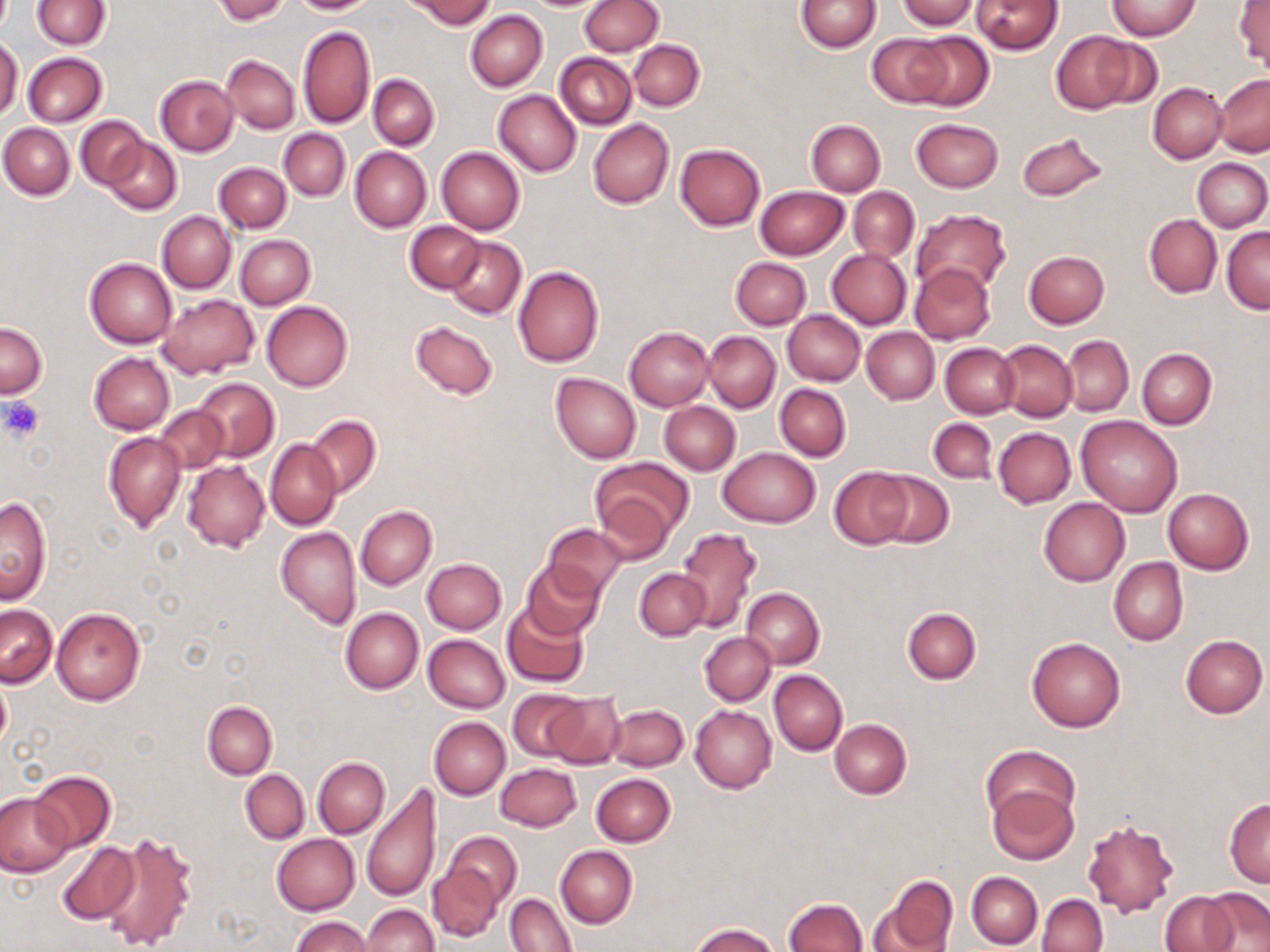

Approximate bounding boxes as [x1, y1, x2, y2] in pixels. Uninfected red blood cell locations: [31, 0, 111, 49], [212, 0, 289, 23], [288, 0, 379, 15], [407, 0, 496, 28], [581, 0, 663, 55], [797, 0, 881, 53], [897, 0, 979, 31], [972, 0, 1063, 54], [1106, 1, 1202, 39], [1233, 2, 1269, 72], [465, 10, 546, 92], [297, 26, 375, 129], [1051, 31, 1140, 113], [907, 32, 995, 110], [866, 33, 953, 107], [1087, 34, 1166, 110], [0, 36, 23, 120], [628, 39, 704, 110], [23, 53, 107, 127], [554, 53, 636, 129], [221, 55, 299, 133], [159, 65, 296, 142], [368, 75, 438, 150], [1214, 75, 1270, 157], [156, 76, 238, 156], [1148, 83, 1227, 163], [494, 89, 581, 176], [76, 116, 147, 191], [588, 118, 674, 208], [912, 118, 1003, 192], [806, 120, 885, 195], [1, 123, 74, 199], [279, 129, 350, 200], [1018, 130, 1107, 202], [105, 138, 182, 214], [674, 144, 765, 231], [350, 146, 431, 232], [436, 146, 525, 234], [1193, 158, 1270, 231], [214, 162, 291, 233], [755, 186, 849, 259], [849, 187, 920, 262], [912, 209, 1011, 295], [157, 211, 236, 292], [1144, 214, 1222, 297], [405, 221, 485, 293], [1221, 226, 1270, 314], [234, 235, 315, 309], [445, 237, 526, 319], [827, 248, 911, 329], [1024, 250, 1109, 327], [84, 257, 177, 348], [730, 257, 811, 329], [910, 262, 996, 344], [514, 265, 604, 367], [158, 294, 258, 378], [261, 300, 353, 391], [783, 309, 865, 386], [411, 320, 498, 400], [1, 321, 48, 397], [625, 327, 713, 410], [861, 327, 939, 404], [702, 331, 780, 412], [1061, 337, 1134, 416], [997, 340, 1077, 421], [940, 342, 1020, 417], [1137, 348, 1216, 428], [88, 352, 174, 434], [551, 372, 641, 463], [193, 377, 278, 461], [775, 383, 851, 461], [659, 401, 741, 475], [156, 406, 228, 473], [306, 415, 381, 496], [1077, 416, 1183, 515], [928, 418, 997, 484], [994, 428, 1075, 507], [104, 432, 186, 531], [266, 440, 341, 531], [718, 447, 820, 526], [590, 458, 692, 549], [183, 460, 270, 551], [829, 466, 914, 547], [872, 469, 953, 547], [1164, 489, 1254, 574], [0, 497, 51, 603], [1038, 498, 1129, 587], [355, 505, 437, 590], [544, 523, 629, 597], [275, 525, 361, 629], [675, 527, 762, 631], [1109, 557, 1188, 645], [423, 559, 506, 634], [521, 559, 606, 640], [634, 567, 709, 639], [741, 588, 826, 669], [502, 602, 590, 688], [0, 605, 57, 687], [52, 607, 146, 706], [902, 607, 981, 684], [340, 608, 423, 692], [700, 632, 775, 706], [423, 633, 510, 713], [1180, 634, 1268, 717], [1027, 637, 1125, 731], [768, 670, 848, 755], [1, 675, 12, 753], [507, 688, 587, 763], [543, 692, 626, 769], [203, 701, 277, 778], [606, 703, 689, 771], [690, 705, 776, 794], [430, 717, 510, 799], [830, 718, 911, 799], [982, 745, 1078, 826], [314, 757, 390, 838], [496, 763, 581, 831], [240, 769, 310, 844], [30, 771, 115, 851], [591, 773, 675, 847], [988, 783, 1077, 864], [362, 784, 442, 905], [0, 792, 72, 876], [1225, 799, 1270, 887], [1082, 817, 1181, 918], [446, 831, 521, 905], [99, 833, 199, 952], [272, 834, 359, 914], [55, 841, 139, 925], [555, 845, 638, 927], [426, 862, 503, 942], [967, 871, 1042, 949], [874, 875, 958, 951], [1201, 888, 1270, 951], [1160, 892, 1236, 952], [506, 893, 577, 952], [1038, 893, 1107, 952], [783, 898, 867, 952], [363, 904, 438, 952], [290, 916, 372, 951], [690, 924, 778, 952]. Platelet locations: [1, 395, 44, 440]. Slide-level diagnosis: no evidence of blood parasites. Optical microscopy. Captured at 1000x magnification. Thin blood smear. Image is 1270×952 pixels. One field of a larger specimen. May-Grünwald-Giemsa stain.